Locate and identify every blood parasite.
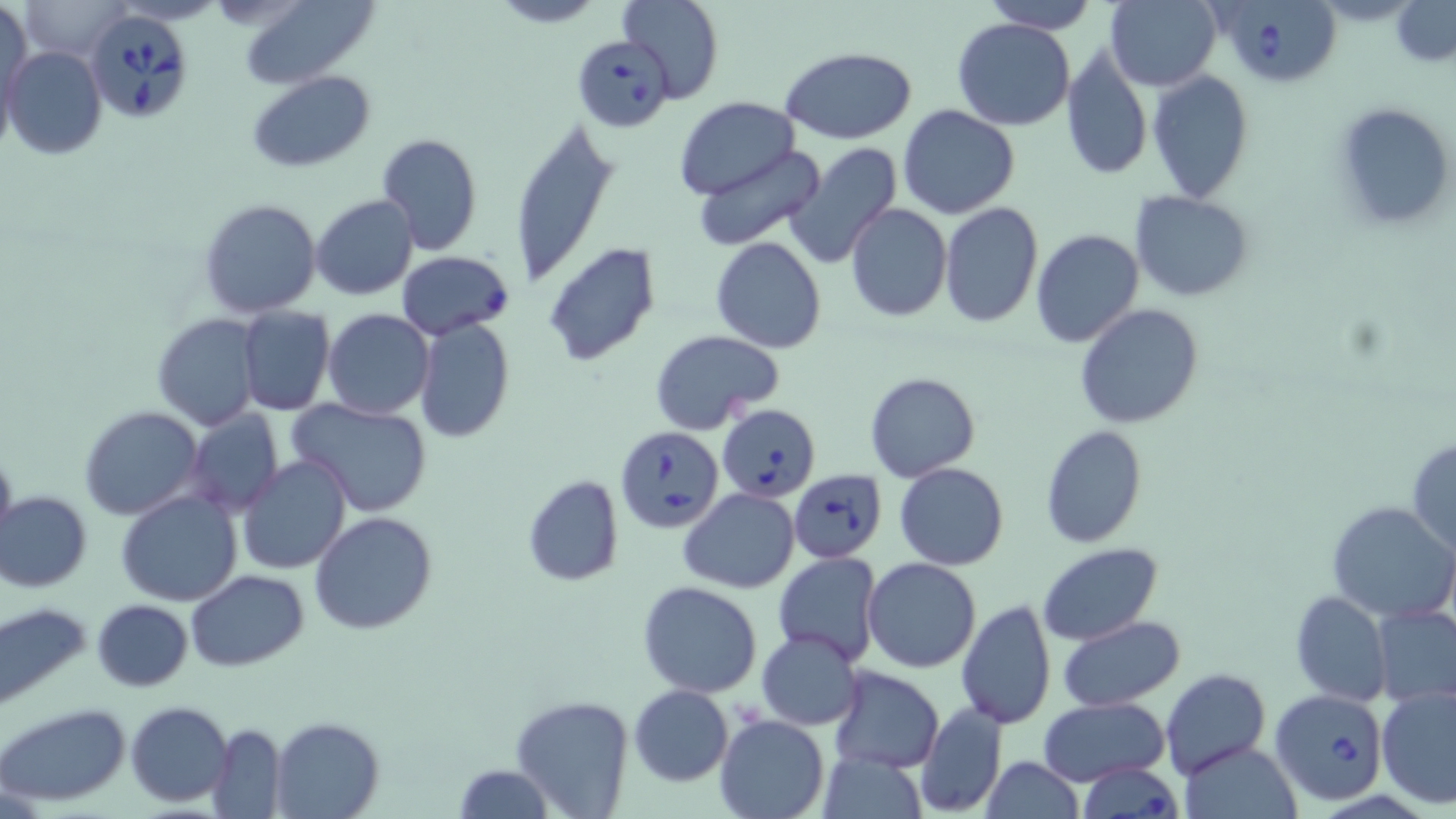

Approximate bounding boxes as (x1,y1)-(x2,y2) corner pairs in pixels.
Babesia divergens-infected red blood cells: (1223,0)-(1343,86), (82,7)-(196,123), (572,37)-(672,133), (397,251)-(515,340), (721,406)-(822,500), (617,430)-(724,536), (787,467)-(888,563), (1272,689)-(1390,806), (1077,762)-(1184,819).
No Plasmodium falciparum, Plasmodium ovale, Plasmodium malariae, Plasmodium vivax, or Trypanosoma brucei observed.

slide-level diagnosis = Babesia divergens
field of view = one of a larger specimen
uninfected red blood cell locations = approximate bounding boxes as (x1,y1)-(x2,y2) corner pairs in pixels: (237,0)-(380,89), (487,0)-(607,28), (616,0)-(723,105), (983,0)-(1094,32), (1104,0)-(1221,91), (1391,0)-(1456,66), (1,1)-(33,118), (953,17)-(1074,132), (1062,43)-(1153,182), (3,46)-(107,160), (781,48)-(918,142), (1146,70)-(1255,202), (249,71)-(375,172), (673,96)-(800,199), (1332,100)-(1454,234), (898,106)-(1019,219), (507,116)-(618,287), (375,133)-(482,257), (783,144)-(904,268), (693,146)-(827,253), (1131,191)-(1254,301), (310,194)-(418,300), (197,197)-(323,319), (939,203)-(1043,328), (845,204)-(952,321), (1031,229)-(1144,348), (710,237)-(827,353), (543,242)-(661,367), (1075,303)-(1207,429), (238,307)-(335,416), (323,309)-(434,420), (152,314)-(261,430), (413,318)-(515,443), (649,328)-(786,435), (865,372)-(981,482), (287,397)-(434,518), (79,406)-(202,520), (188,410)-(285,513), (1039,425)-(1147,547), (1407,437)-(1456,555), (0,443)-(17,554), (239,454)-(352,575), (895,462)-(1008,569), (521,474)-(624,587), (679,488)-(800,594), (115,491)-(242,608), (1,492)-(91,592), (1326,500)-(1455,625), (309,511)-(439,634), (1036,542)-(1163,646), (773,552)-(885,669), (862,557)-(982,673), (186,569)-(309,672), (638,580)-(763,698), (1290,590)-(1391,708), (955,598)-(1056,730), (92,599)-(191,692), (1,602)-(92,711), (1372,603)-(1456,707), (1058,615)-(1185,709), (756,629)-(863,730), (828,667)-(944,772), (1159,668)-(1270,778), (627,684)-(732,786), (1375,685)-(1456,810), (839,689)-(1000,803), (510,694)-(635,819), (1038,698)-(1169,786), (126,700)-(233,805), (0,702)-(132,808), (915,704)-(1007,817), (715,713)-(830,818), (270,717)-(384,819), (207,724)-(285,817), (1177,740)-(1304,819), (818,750)-(926,818), (981,758)-(1086,818), (453,764)-(554,819)
preparation = thin blood film
stain = May-Grünwald-Giemsa
magnification = 1000x
image size = 1456×819 pixels
modality = light microscopy